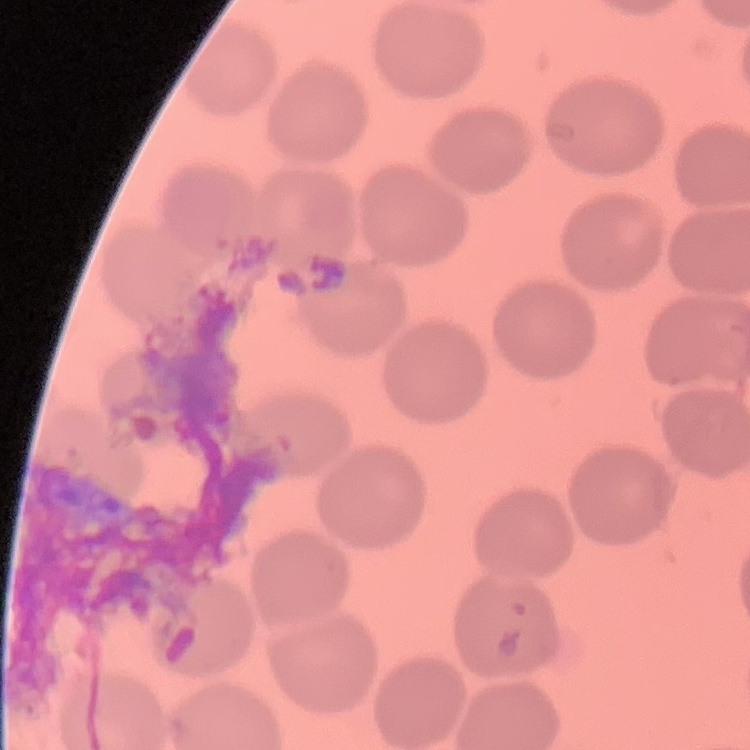

Summary:
  - Erythrocyte morphology: no rouleaux formation
  - Stain: Field's or Giemsa
  - Preparation: thin blood film
  - Image type: square crop of a larger photomicrograph